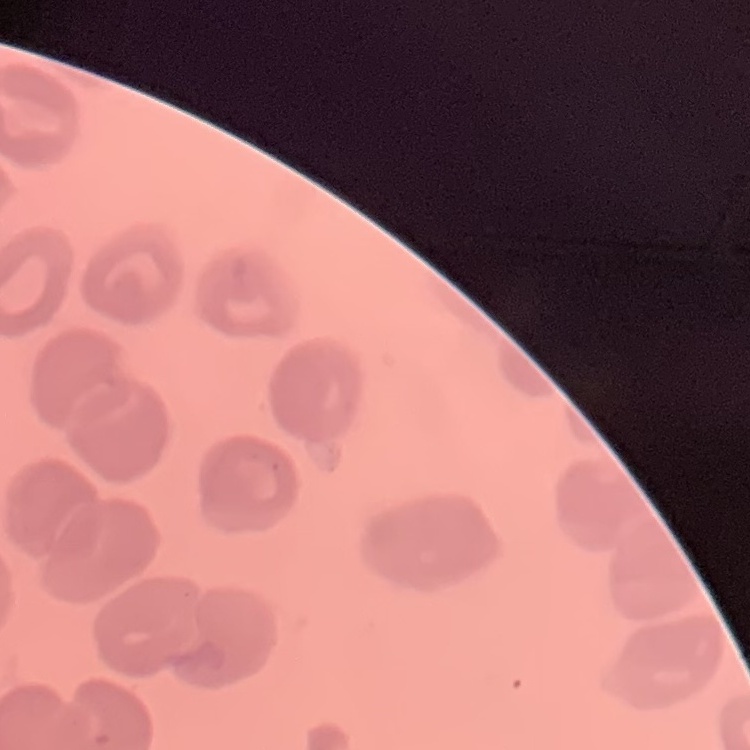

erythrocyte morphology = no rouleaux formation
stain = Field's or Giemsa
image type = square crop of a larger photomicrograph
preparation = thin peripheral smear